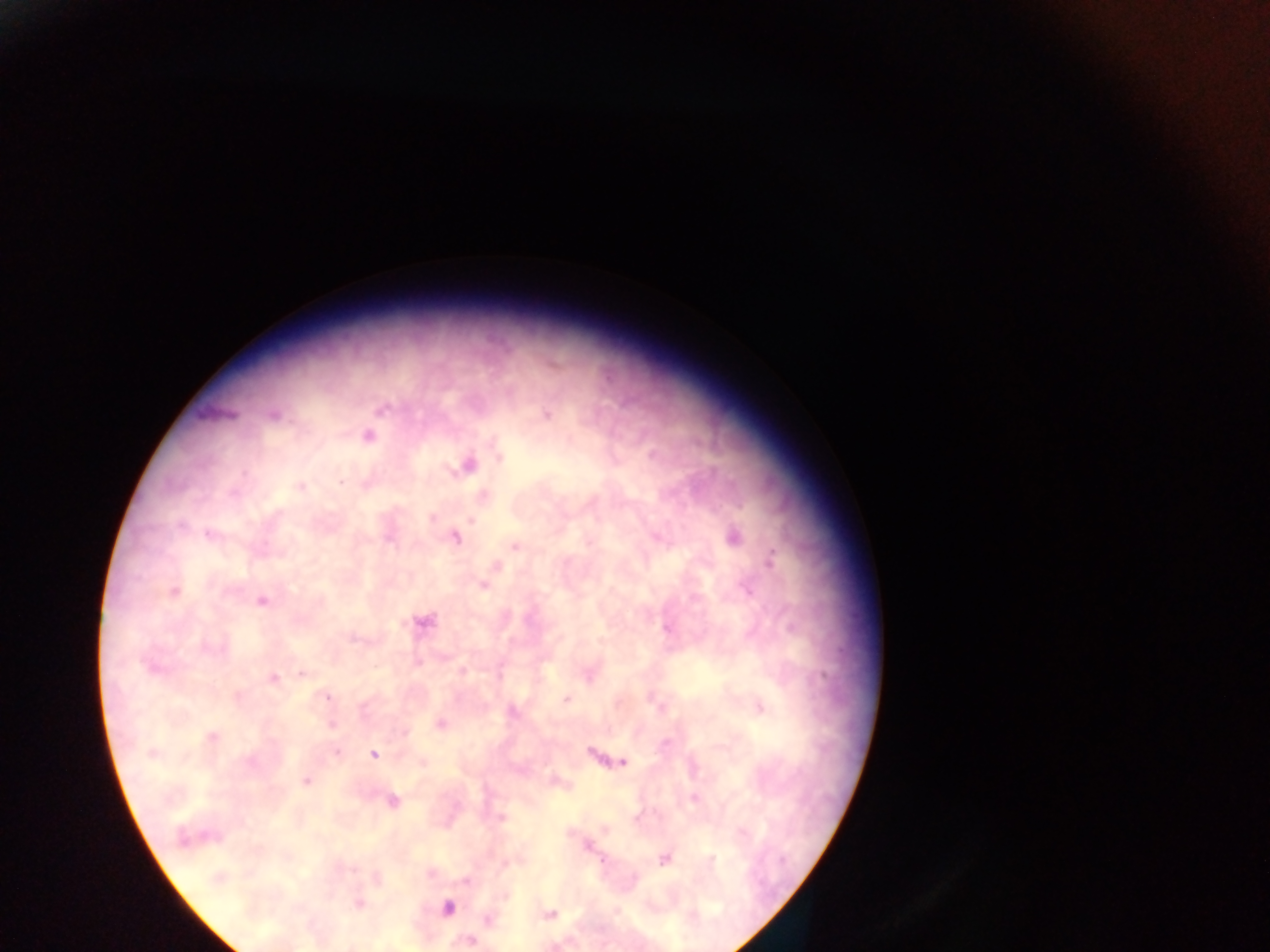

Approximate centers as x y in pixels.
Summary:
  - Malaria parasite locations: 381 407; 545 414; 274 415; 367 436; 498 453; 467 464; 300 486; 482 495; 432 518; 208 534; 656 536; 732 536; 454 537; 515 546; 770 559; 494 566; 482 584; 172 591; 261 600; 422 621; 152 666; 463 671; 588 672; 303 673; 273 678; 238 694; 566 699; 758 707; 331 723; 440 724; 210 737; 336 751; 151 753; 592 754; 373 755; 622 761; 422 763; 306 779; 554 783; 694 798; 391 801; 500 818; 606 829; 185 837; 587 846; 664 859; 218 878; 376 878; 358 903; 447 908; 549 915; 488 919; 471 940; 352 945
  - Preparation: thick blood film
  - Image size: 1270×952 pixels
  - Field of view: single
  - Capture: mobile-phone photograph through a microscope
  - Country: Ghana